Mark where leukocytes are.
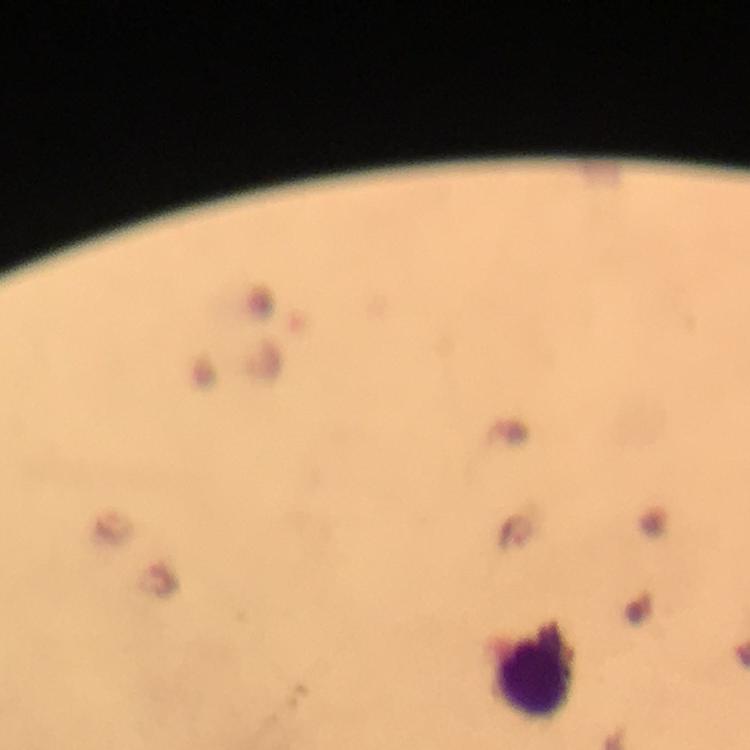

Approximate centers as {x, y} in pixels.
Leukocytes: {535, 669}.

Summary:
  - Magnification: 100x
  - Stain: Giemsa
  - Capture: smartphone photograph through a microscope
  - Context: from a malaria diagnostic workup
  - Plasmodium parasites: none seen
  - Cropped from: one field of view
  - Preparation: thick blood smear
  - Image size: 750×750 pixels
  - Immersion oil: applied